Identify the parasite.
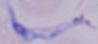
This is a trypanosome.

Summary:
  - Magnification: 1000x
  - Modality: micrograph